Classify this cell by malaria status.
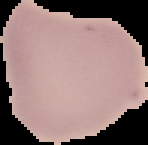
Uninfected.

{
  "image_type": "segmented cell region on a black background",
  "image_size": "148×145 pixels",
  "preparation": "thin blood film"
}